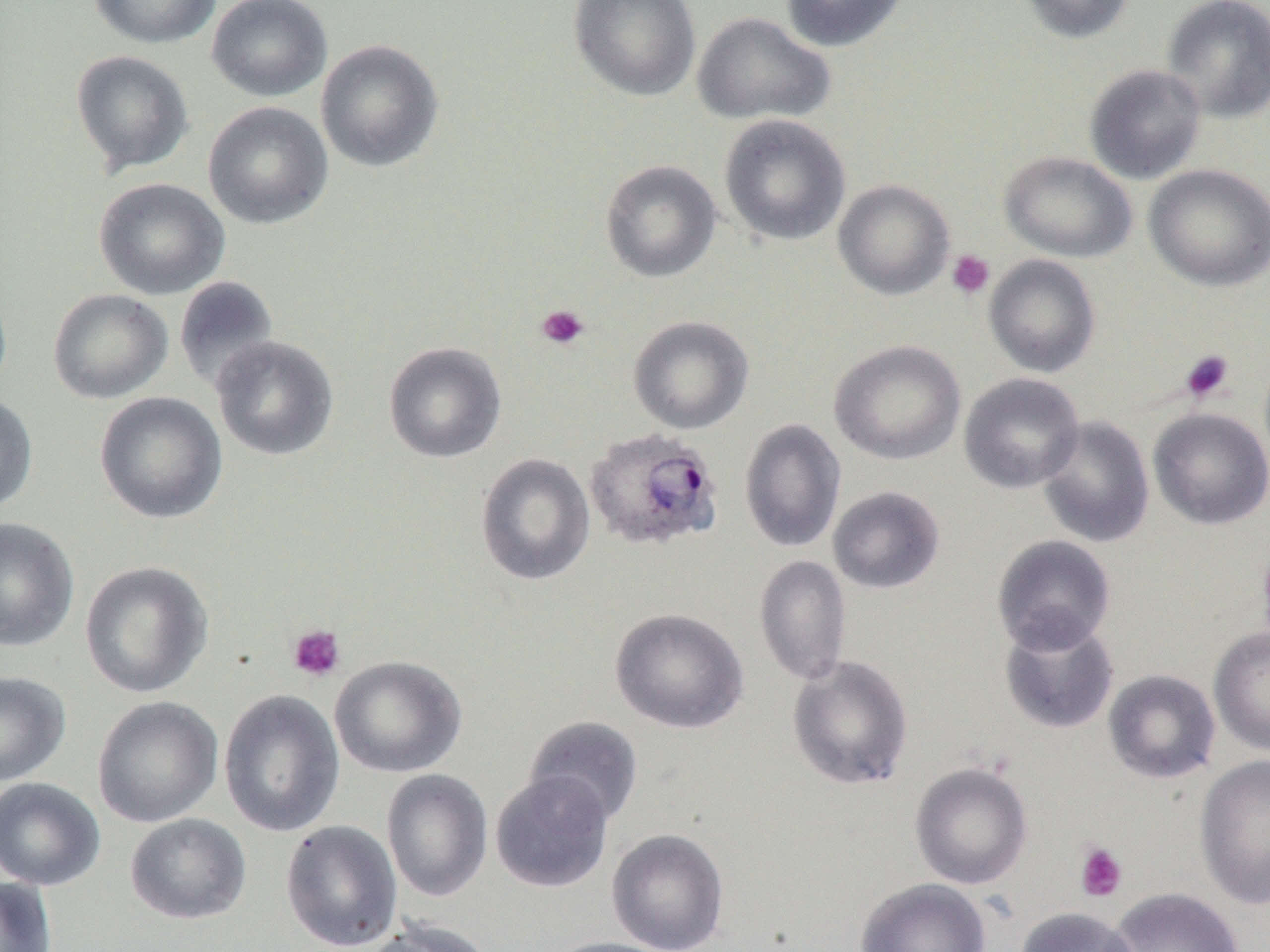 Approximate bounding boxes as named x1/y1/x2/y2 corners in pixels. Plasmodium ovale-infected red blood cell locations: (x1=584, y1=427, x2=724, y2=552). Platelet locations: (x1=946, y1=250, x2=995, y2=299), (x1=536, y1=303, x2=590, y2=350), (x1=1179, y1=349, x2=1235, y2=403), (x1=287, y1=623, x2=346, y2=682), (x1=1074, y1=841, x2=1127, y2=902). Uninfected red blood cell locations: (x1=89, y1=0, x2=222, y2=49), (x1=206, y1=0, x2=333, y2=102), (x1=568, y1=0, x2=701, y2=102), (x1=780, y1=0, x2=910, y2=52), (x1=1018, y1=0, x2=1136, y2=44), (x1=1161, y1=0, x2=1270, y2=123), (x1=691, y1=11, x2=835, y2=126), (x1=315, y1=39, x2=445, y2=172), (x1=70, y1=50, x2=194, y2=175), (x1=1084, y1=64, x2=1206, y2=184), (x1=203, y1=101, x2=334, y2=230), (x1=718, y1=114, x2=851, y2=246), (x1=998, y1=151, x2=1137, y2=263), (x1=600, y1=159, x2=722, y2=283), (x1=1143, y1=164, x2=1270, y2=292), (x1=93, y1=177, x2=230, y2=300), (x1=833, y1=179, x2=955, y2=300), (x1=983, y1=254, x2=1101, y2=378), (x1=174, y1=276, x2=280, y2=394), (x1=47, y1=288, x2=173, y2=404), (x1=628, y1=315, x2=754, y2=434), (x1=211, y1=335, x2=340, y2=461), (x1=829, y1=339, x2=966, y2=466), (x1=383, y1=341, x2=507, y2=463), (x1=959, y1=373, x2=1085, y2=493), (x1=0, y1=392, x2=39, y2=514), (x1=94, y1=392, x2=228, y2=524), (x1=1148, y1=407, x2=1270, y2=530), (x1=1037, y1=415, x2=1155, y2=548), (x1=739, y1=419, x2=846, y2=553), (x1=475, y1=452, x2=596, y2=586), (x1=827, y1=486, x2=946, y2=594), (x1=0, y1=517, x2=79, y2=652), (x1=992, y1=535, x2=1116, y2=653), (x1=754, y1=555, x2=852, y2=687), (x1=79, y1=561, x2=213, y2=699), (x1=610, y1=607, x2=749, y2=733), (x1=998, y1=614, x2=1119, y2=735), (x1=1209, y1=626, x2=1270, y2=756), (x1=786, y1=654, x2=914, y2=790), (x1=329, y1=655, x2=468, y2=778), (x1=1103, y1=669, x2=1221, y2=784), (x1=0, y1=671, x2=71, y2=785), (x1=218, y1=689, x2=345, y2=837), (x1=92, y1=696, x2=223, y2=828), (x1=523, y1=716, x2=644, y2=825), (x1=1194, y1=753, x2=1270, y2=909), (x1=910, y1=762, x2=1033, y2=889), (x1=382, y1=768, x2=493, y2=903), (x1=490, y1=770, x2=614, y2=893), (x1=0, y1=777, x2=105, y2=891), (x1=125, y1=813, x2=251, y2=924), (x1=280, y1=819, x2=402, y2=952), (x1=606, y1=828, x2=730, y2=952), (x1=0, y1=876, x2=57, y2=951), (x1=854, y1=878, x2=991, y2=952), (x1=1108, y1=887, x2=1244, y2=951), (x1=1015, y1=906, x2=1139, y2=952), (x1=361, y1=919, x2=494, y2=952), (x1=544, y1=936, x2=680, y2=952). Slide-level diagnosis: Plasmodium ovale. 1000x magnification. Single field of view. Image is 1270×952 pixels. Thin blood film. Light microscopy.